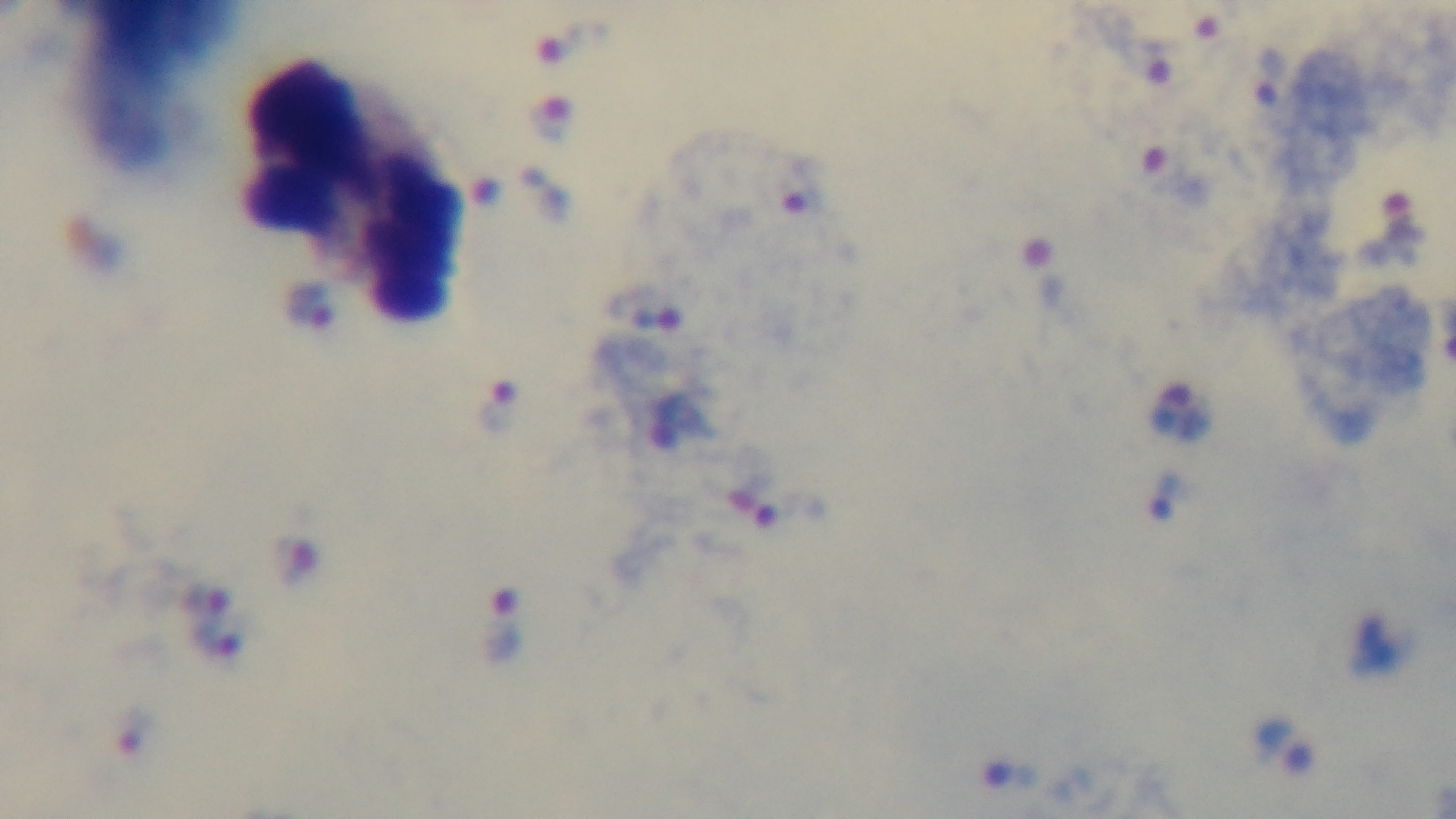

Summary:
  - Modality: light microscopy
  - Malaria status: positive
  - Field of view: single
  - Preparation: thick
  - Objective: 100x oil immersion
  - Capture: mounted 4K digital camera
  - Stain: Giemsa